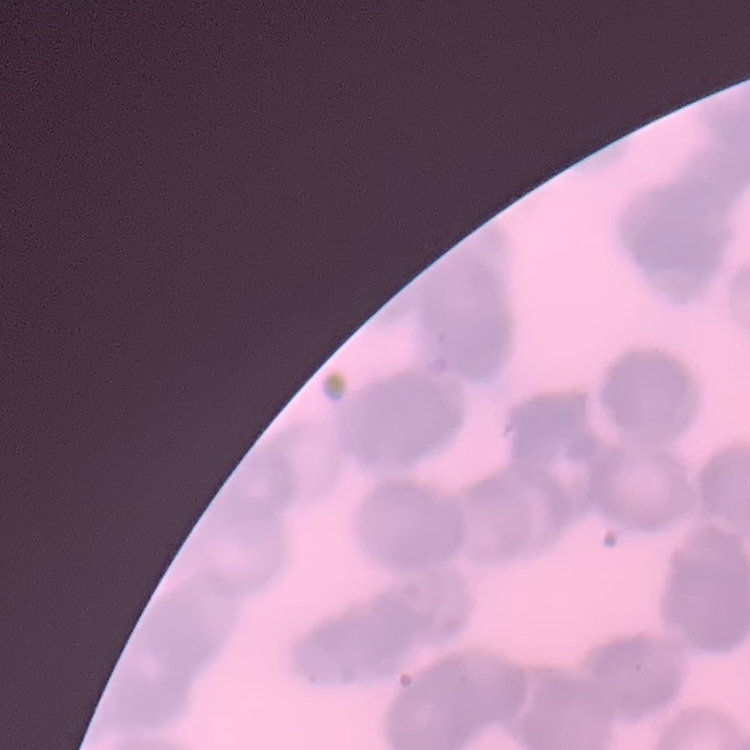
red blood cell morphology = rouleaux formation
image type = one tile cut from a larger photomicrograph
stain = Field's or Giemsa
preparation = thin peripheral smear